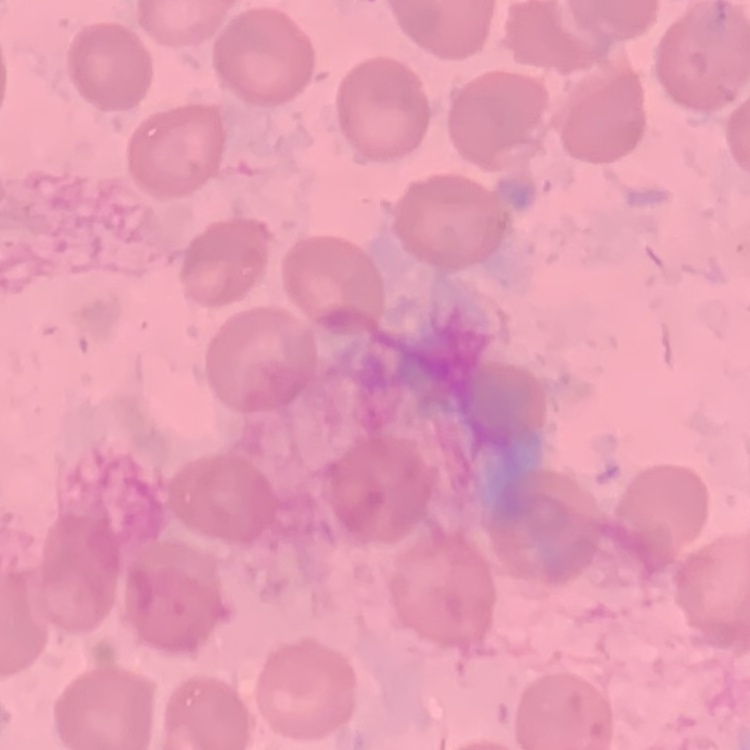
Summary:
  - Erythrocyte morphology: no rouleaux formation
  - Image type: square crop of a larger photomicrograph
  - Stain: Field's or Giemsa
  - Preparation: thin blood smear